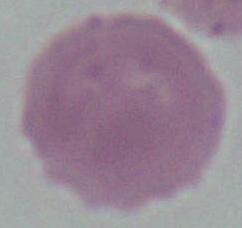

identification = red blood cell
modality = photomicrograph
magnification = 1000x